Identify the cell.
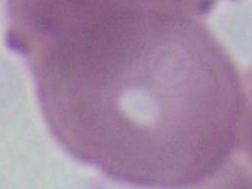
This is an erythrocyte.

Captured at 1000x magnification. Photomicrograph.